Comment on the morphology of the red blood cells.
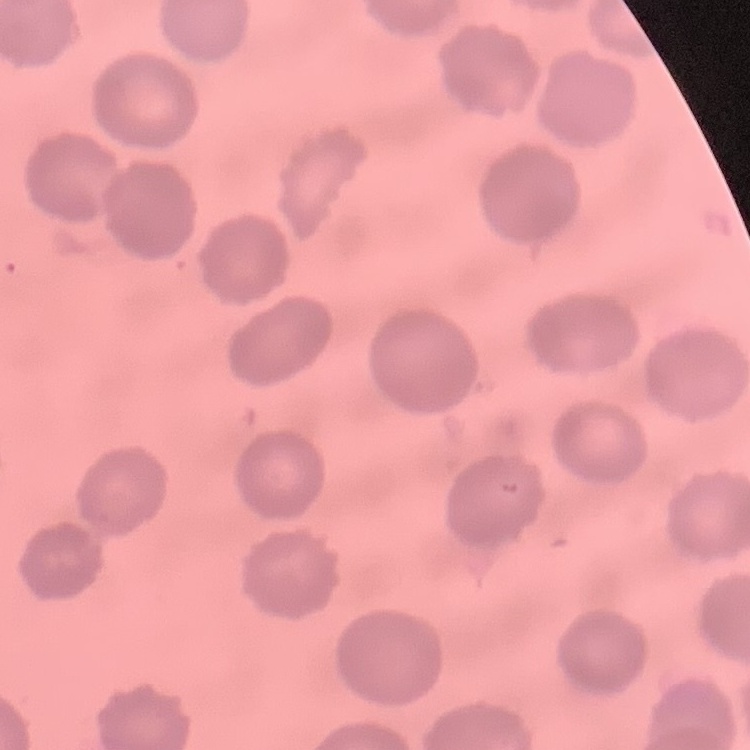

They show no rouleaux formation.

{
  "stain": "Field's or Giemsa",
  "preparation": "thin blood film",
  "image_type": "one tile cut from a larger photomicrograph"
}